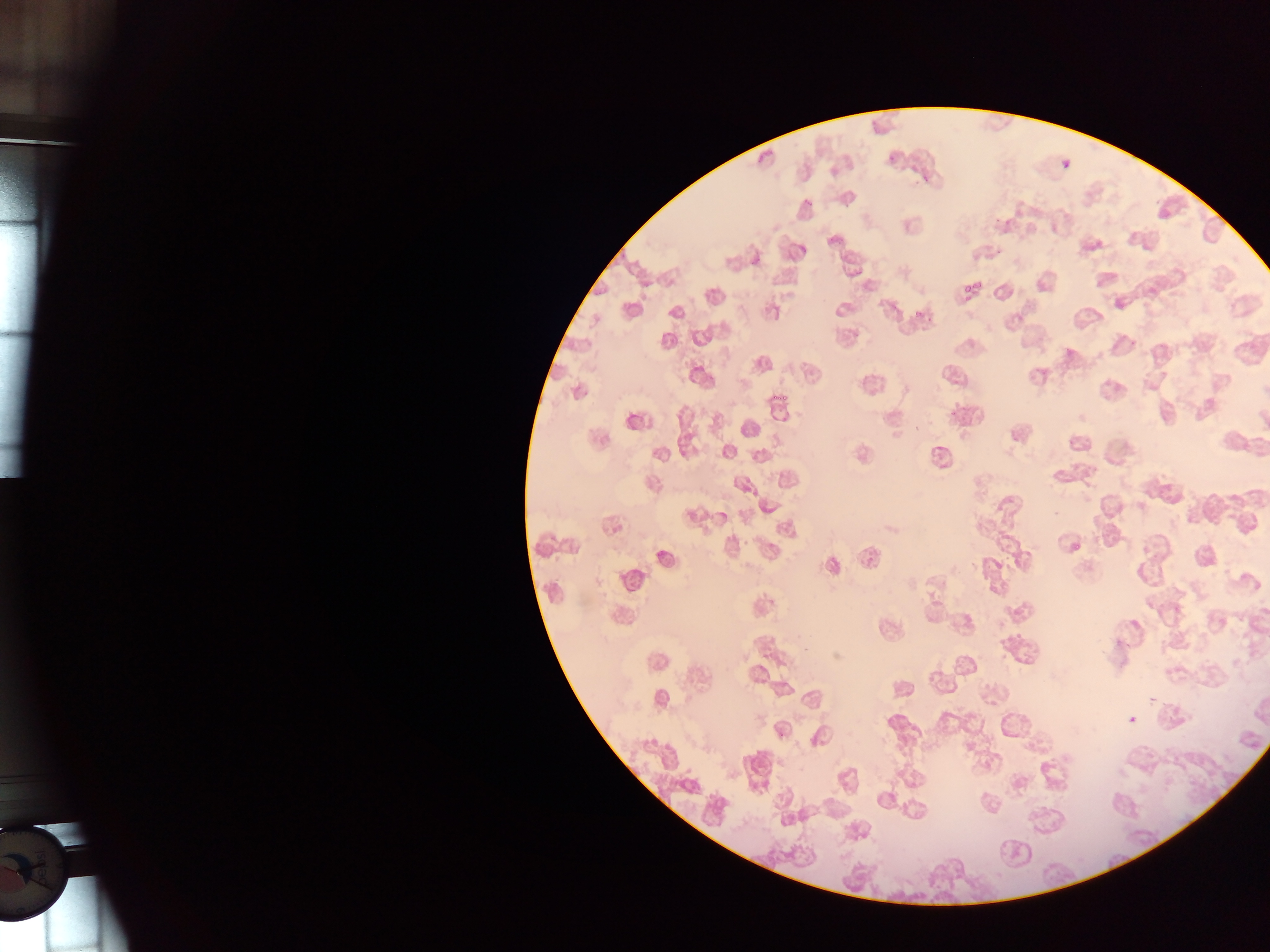

capture: mobile-phone photograph through a microscope
field_of_view: single
country: Ghana
image_size: 1270×952 pixels
preparation: thin blood film
plasmodium_parasite_locations: 'approximate bounding boxes as [left, top, right, bottom] in pixels: [888, 154, 898, 163], [1063, 160, 1071, 168], [920, 169, 932, 187], [802, 196, 814, 205], [994, 212, 1006, 228], [994, 247, 1007, 258], [961, 278, 980, 295], [960, 290, 977, 304], [916, 304, 926, 316], [1127, 335, 1141, 344], [770, 391, 790, 403], [948, 407, 962, 420], [1075, 543, 1081, 551]'